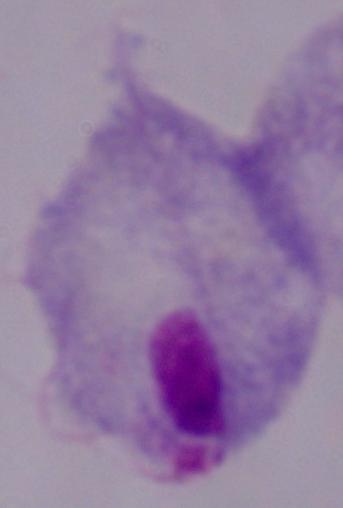
Summary:
  - Magnification: 1000x
  - Modality: micrograph
  - Identification: trichomonad